Classify this cell by malaria status.
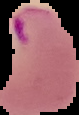

Parasitized.

{
  "image_size": "79×115 pixels",
  "preparation": "thin blood smear",
  "image_type": "cell region segmented out of the field of view; surrounding area masked to black"
}